Locate every blood parasite and identify its species.
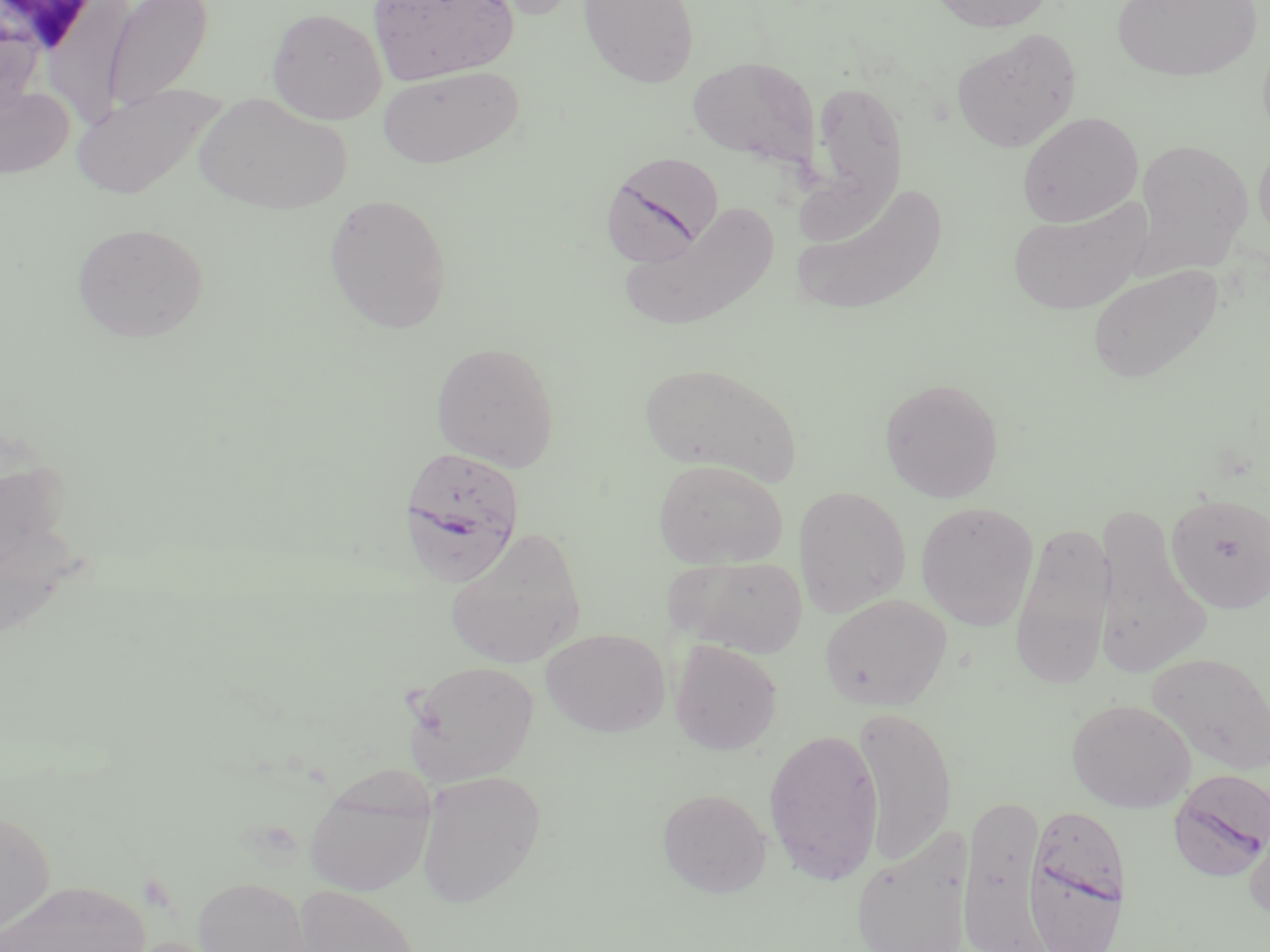

Approximate bounding boxes as [x1, y1, x2, y2] in pixels.
Plasmodium falciparum-infected red blood cells: [601, 153, 724, 266], [397, 445, 527, 587], [1168, 770, 1270, 881], [1025, 814, 1123, 952].
No Plasmodium ovale, Plasmodium malariae, Plasmodium vivax, Babesia divergens, or Trypanosoma brucei observed.

Summary:
  - Uninfected red blood cell locations: [103, 0, 213, 113], [368, 0, 518, 85], [458, 0, 583, 21], [578, 0, 699, 88], [927, 0, 1057, 32], [45, 1, 133, 124], [1111, 1, 1262, 82], [267, 6, 387, 124], [0, 9, 44, 114], [951, 28, 1082, 154], [687, 55, 822, 171], [377, 65, 523, 168], [810, 79, 908, 211], [0, 84, 75, 179], [70, 84, 224, 201], [194, 94, 354, 215], [1016, 111, 1144, 227], [1254, 137, 1270, 251], [1131, 138, 1253, 277], [790, 180, 949, 318], [323, 193, 453, 334], [1008, 197, 1153, 316], [620, 202, 780, 332], [71, 222, 209, 343], [1086, 263, 1224, 385], [430, 341, 560, 471], [636, 361, 803, 486], [879, 377, 1004, 503], [652, 457, 789, 569], [793, 485, 911, 617], [1166, 492, 1270, 614], [916, 501, 1039, 631], [1093, 506, 1211, 678], [1010, 521, 1115, 691], [445, 527, 587, 669], [666, 554, 808, 657], [819, 594, 952, 711], [541, 628, 670, 737], [670, 640, 783, 755], [1146, 653, 1270, 776], [402, 659, 539, 784], [1066, 698, 1196, 812], [851, 706, 957, 864], [763, 726, 885, 884], [415, 770, 545, 908], [304, 775, 435, 897], [657, 788, 772, 898], [950, 790, 1056, 952], [0, 807, 57, 940], [1244, 808, 1270, 923], [849, 831, 973, 952], [192, 877, 312, 952], [0, 880, 150, 952], [293, 884, 422, 952], [116, 936, 229, 952]
  - Slide-level diagnosis: Plasmodium falciparum
  - Image size: 1270×952 pixels
  - Stain: May-Grünwald-Giemsa
  - Magnification: 1000x
  - Preparation: thin blood film
  - Field of view: single
  - Modality: optical microscopy